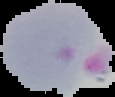

image size = 115×97 pixels
malaria status = parasitized
image type = cell region segmented out of the field of view; surrounding area masked to black
preparation = thin blood smear